Point out each Plasmodium parasite.
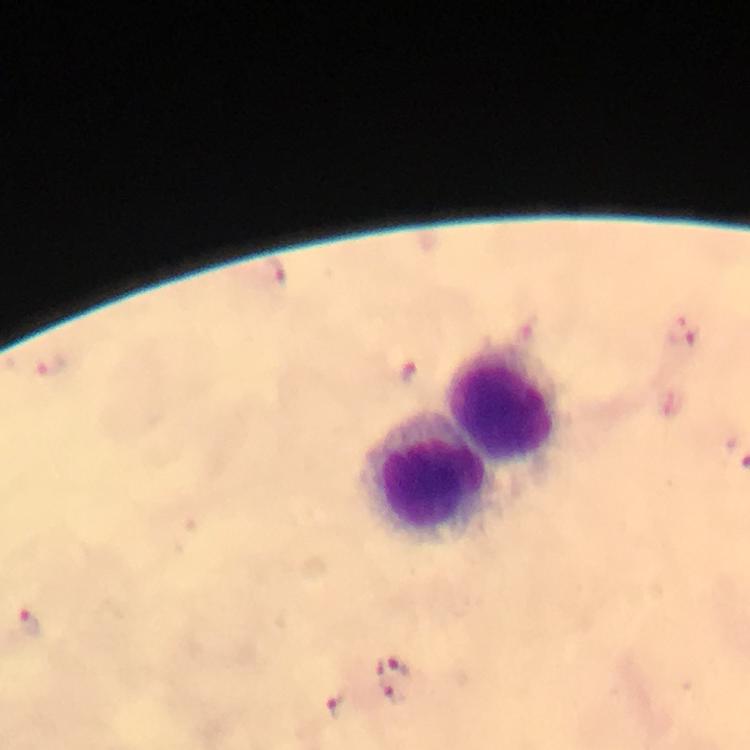

Approximate object centers, in pixels from the top-left corner.
Plasmodium parasites: (x=277, y=277), (x=684, y=332), (x=48, y=367), (x=414, y=372), (x=29, y=623), (x=396, y=669), (x=392, y=686), (x=337, y=704).

Leukocyte locations: (x=508, y=401), (x=428, y=474). Smartphone photograph taken through a microscope. From a diagnostic examination for malaria. Immersion oil applied. Giemsa stain. Image is 750×750 pixels. Thick smear. 100x magnification. A crop from one field of view.